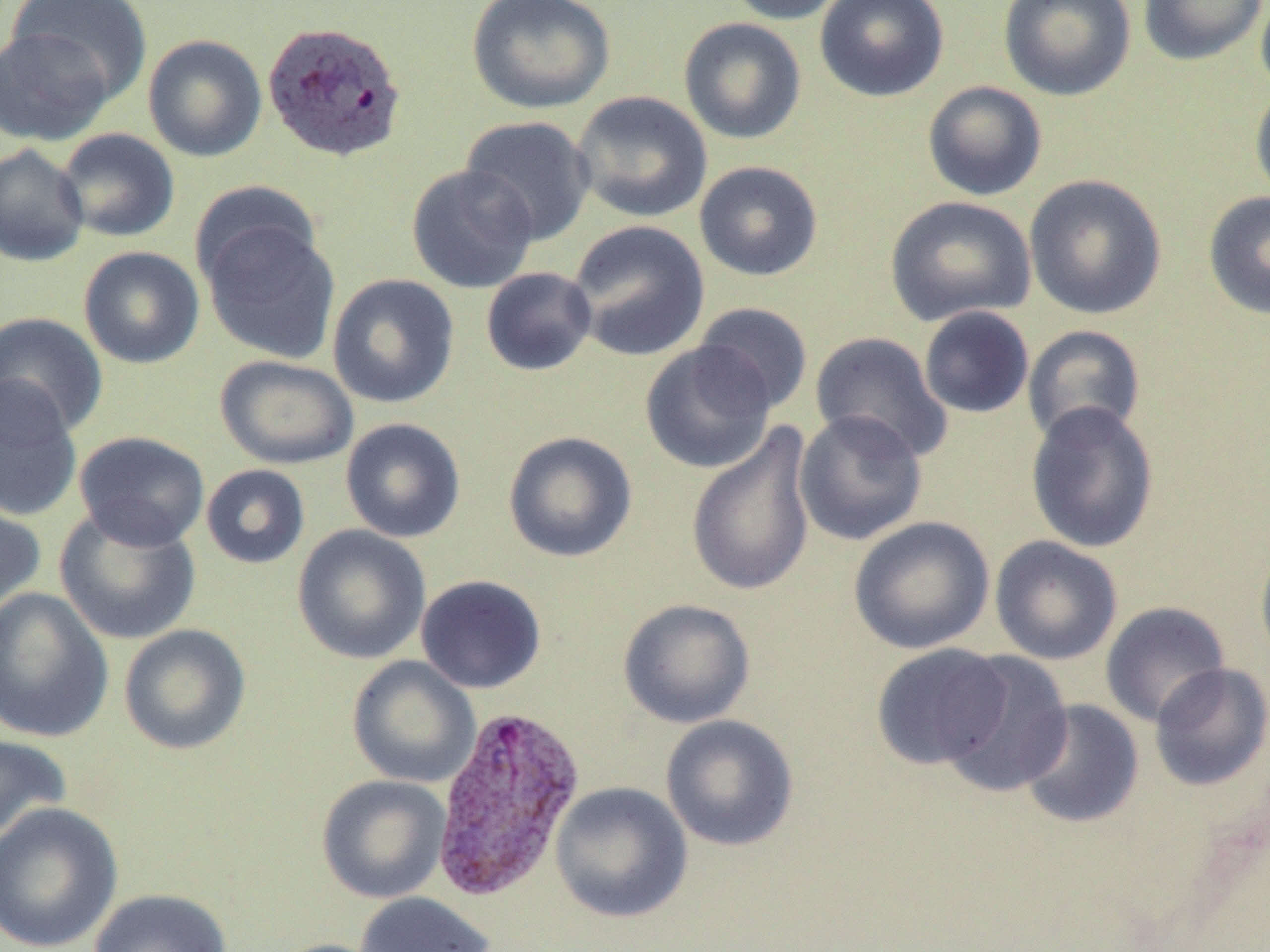

Approximate bounding boxes as (x1, y1, x2, y2) in pixels. Plasmodium vivax-infected red blood cell locations: (261, 21, 408, 162), (430, 703, 587, 903). Uninfected red blood cell locations: (7, 0, 154, 102), (466, 0, 616, 114), (722, 0, 850, 25), (814, 0, 950, 102), (997, 0, 1136, 101), (1137, 0, 1268, 65), (1255, 0, 1270, 97), (678, 17, 807, 145), (0, 26, 114, 146), (142, 34, 267, 162), (921, 80, 1047, 201), (1250, 83, 1270, 207), (571, 91, 712, 223), (459, 115, 596, 245), (56, 129, 180, 243), (0, 143, 90, 267), (694, 160, 824, 281), (406, 163, 539, 293), (1023, 173, 1167, 320), (191, 180, 323, 291), (1203, 191, 1270, 321), (884, 195, 1037, 327), (200, 218, 341, 364), (568, 219, 710, 361), (79, 246, 205, 369), (480, 267, 597, 376), (326, 273, 460, 409), (693, 302, 813, 414), (918, 305, 1035, 419), (0, 312, 108, 436), (1022, 324, 1147, 445), (809, 331, 953, 464), (640, 341, 776, 474), (215, 355, 359, 470), (0, 375, 83, 522), (1024, 401, 1160, 554), (793, 409, 928, 546), (340, 417, 466, 543), (685, 424, 817, 598), (73, 430, 210, 550), (502, 430, 638, 563), (200, 464, 310, 569), (0, 493, 46, 615), (54, 506, 202, 646), (848, 516, 995, 654), (292, 524, 431, 665), (989, 535, 1123, 665), (1255, 539, 1270, 670), (415, 574, 546, 694), (0, 587, 115, 744), (617, 598, 755, 728), (1100, 601, 1230, 727), (118, 623, 252, 755), (870, 643, 1012, 771), (935, 650, 1074, 797), (347, 656, 481, 789), (1149, 662, 1270, 791), (1017, 699, 1144, 829), (660, 714, 800, 852), (0, 735, 72, 845), (316, 774, 452, 904), (549, 781, 693, 924), (1, 802, 123, 952), (88, 888, 232, 951), (354, 892, 497, 952), (268, 938, 393, 952). Slide-level diagnosis: Plasmodium vivax. 1000x magnification. Image is 1270×952 pixels. Light microscopy. Single field of view. Thin blood film.